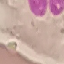
result = no malaria parasites seen
stain = Giemsa
image type = automatically extracted cell patch, resized to 64 × 64 pixels
preparation = thin smear
capture = smartphone camera at the microscope eyepiece